Locate every blood parasite and identify its species.
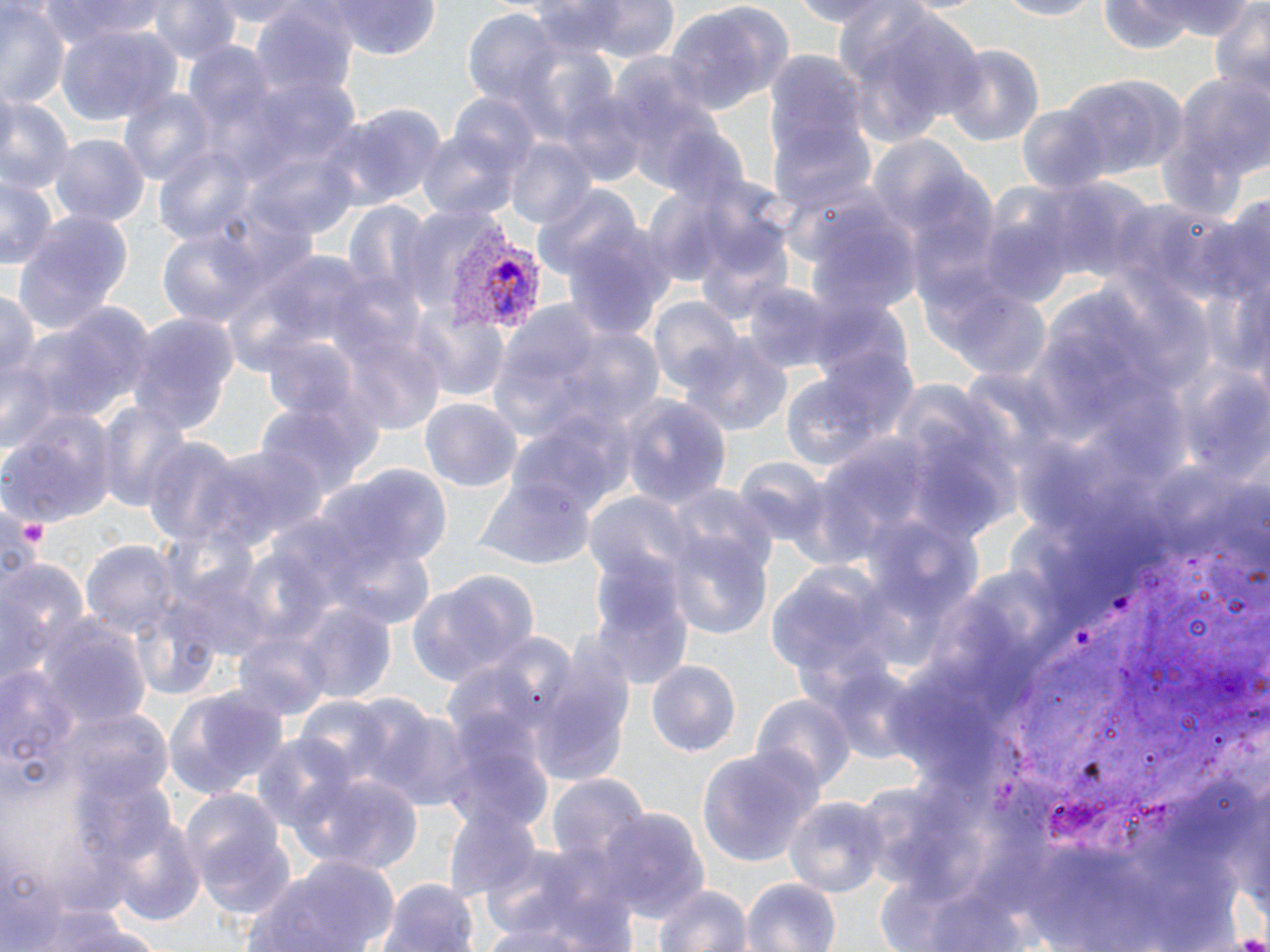
Approximate bounding boxes as (x1, y1, x2, y2) in pixels.
Plasmodium vivax-infected red blood cells: (448, 234, 544, 332).
No Plasmodium falciparum, Plasmodium ovale, Plasmodium malariae, Babesia divergens, or Trypanosoma brucei observed.

Platelet locations: (22, 519, 52, 546). Uninfected red blood cell locations: (35, 0, 174, 46), (150, 0, 241, 69), (208, 0, 313, 27), (333, 0, 441, 60), (538, 0, 682, 64), (991, 0, 1099, 20), (1097, 0, 1246, 52), (665, 1, 791, 117), (1208, 1, 1270, 108), (0, 5, 70, 106), (835, 5, 986, 137), (254, 10, 358, 104), (464, 11, 566, 112), (57, 26, 178, 124), (185, 44, 278, 134), (941, 45, 1044, 147), (759, 52, 874, 195), (1158, 68, 1269, 216), (1057, 75, 1188, 179), (117, 88, 218, 190), (559, 91, 649, 183), (449, 92, 544, 187), (0, 93, 72, 196), (335, 104, 447, 209), (1016, 104, 1111, 194), (772, 119, 875, 216), (415, 121, 528, 223), (51, 134, 148, 227), (505, 138, 596, 232), (866, 138, 979, 238), (152, 148, 258, 247), (0, 174, 56, 271), (1032, 178, 1155, 291), (533, 183, 643, 281), (807, 205, 923, 324), (9, 209, 134, 337), (976, 216, 1074, 310), (563, 221, 682, 343), (156, 227, 269, 331), (931, 280, 1053, 385), (744, 282, 849, 377), (0, 285, 40, 394), (646, 297, 743, 394), (484, 299, 642, 449), (17, 303, 152, 433), (408, 306, 511, 400), (128, 313, 237, 431), (261, 334, 364, 424), (681, 337, 792, 438), (775, 373, 887, 479), (420, 396, 521, 491), (619, 396, 731, 513), (97, 401, 194, 514), (255, 402, 364, 511), (0, 407, 115, 526), (144, 436, 245, 543), (201, 441, 327, 553), (734, 458, 831, 549), (312, 466, 450, 575), (475, 475, 594, 567), (665, 487, 778, 587), (586, 492, 693, 585), (664, 528, 774, 644), (81, 539, 180, 644), (328, 540, 436, 630), (0, 559, 86, 685), (588, 563, 696, 694), (180, 565, 275, 662), (408, 569, 538, 686), (297, 602, 395, 703), (36, 618, 153, 735), (529, 651, 635, 788), (645, 660, 742, 762), (163, 685, 287, 802), (754, 695, 854, 796), (295, 697, 392, 785), (371, 706, 473, 811), (63, 709, 175, 808), (441, 718, 554, 834), (253, 735, 358, 839), (697, 745, 822, 868), (296, 770, 426, 871), (547, 773, 650, 868), (180, 786, 296, 919), (783, 794, 885, 896), (441, 804, 542, 902), (598, 810, 708, 923), (106, 811, 207, 928), (239, 854, 403, 951), (480, 855, 633, 951), (741, 875, 842, 952), (381, 878, 480, 952), (649, 881, 753, 952), (11, 901, 162, 952), (480, 910, 624, 950). Slide-level diagnosis: Plasmodium vivax. May-Grünwald-Giemsa stain. Image is 1270×952 pixels. Captured at 1000x magnification. Single field of view. Optical microscopy. Thin blood film.